Locate every Plasmodium falciparum-infected red blood cell.
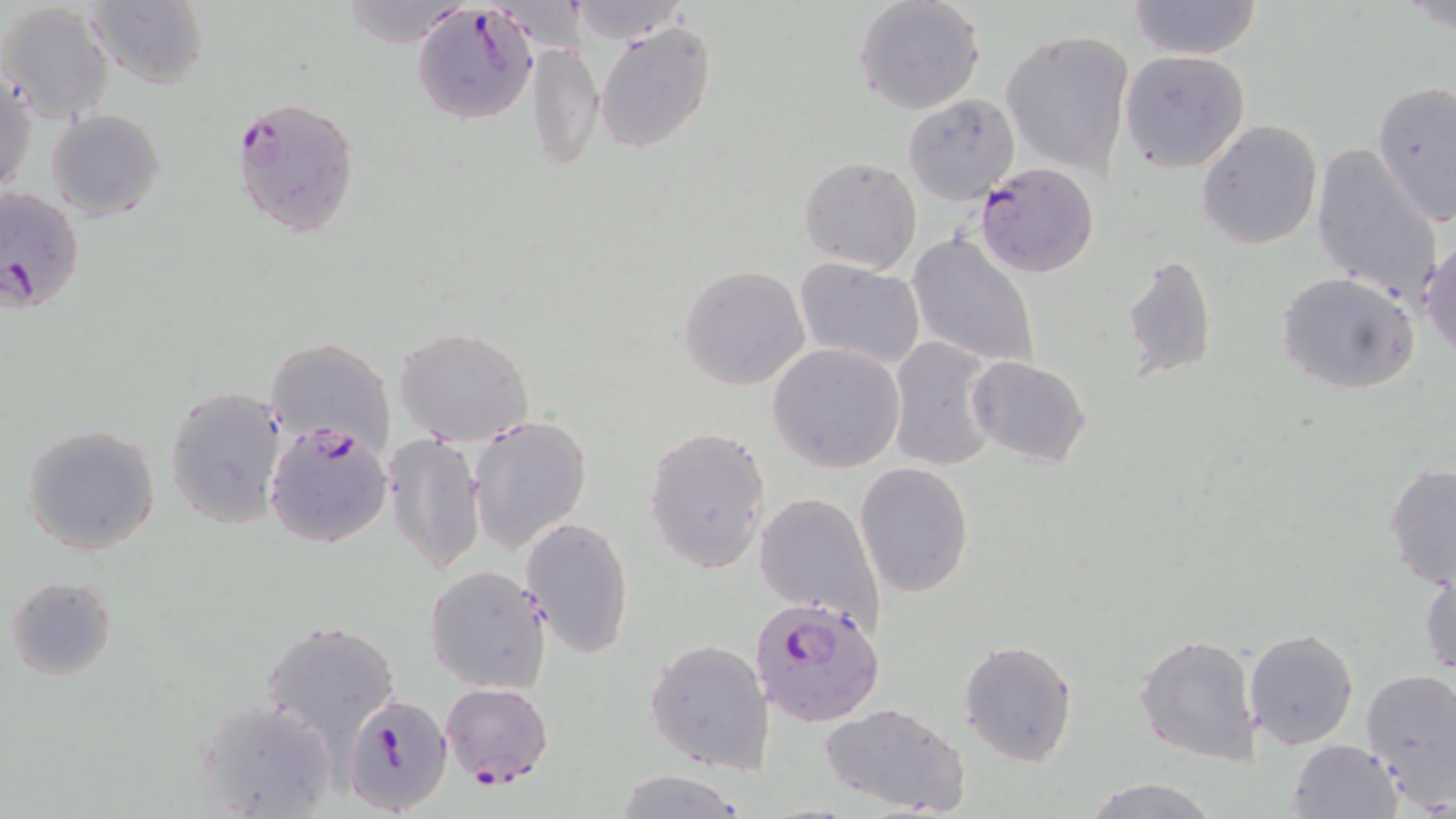

Approximate bounding boxes as [x1, y1, x2, y2] in pixels.
Plasmodium falciparum-infected red blood cells: [412, 3, 545, 127], [229, 94, 360, 237], [975, 161, 1101, 279], [0, 186, 86, 316], [266, 421, 392, 550], [751, 597, 885, 726], [344, 698, 459, 819].

Summary:
  - Uninfected red blood cell locations: [336, 0, 474, 49], [564, 0, 694, 45], [852, 0, 986, 115], [86, 1, 211, 88], [1126, 1, 1264, 62], [1, 2, 113, 122], [593, 20, 717, 155], [998, 30, 1136, 175], [528, 40, 602, 173], [1120, 49, 1252, 174], [1, 72, 35, 199], [1370, 82, 1455, 224], [902, 91, 1018, 204], [47, 109, 164, 222], [1196, 119, 1324, 250], [1311, 143, 1441, 303], [797, 156, 922, 274], [907, 233, 1040, 372], [1420, 236, 1455, 359], [1120, 251, 1218, 382], [795, 261, 925, 370], [678, 264, 810, 391], [1275, 271, 1420, 395], [394, 326, 533, 445], [886, 335, 1004, 473], [267, 338, 397, 452], [769, 344, 905, 473], [966, 355, 1091, 468], [165, 386, 288, 529], [468, 415, 592, 553], [20, 423, 162, 556], [644, 426, 771, 573], [383, 431, 487, 576], [856, 462, 973, 596], [1384, 463, 1456, 592], [754, 490, 885, 629], [520, 515, 635, 658], [1420, 565, 1455, 676], [425, 566, 550, 693], [6, 575, 118, 680], [263, 621, 399, 743], [1243, 628, 1359, 749], [1134, 632, 1260, 765], [645, 637, 774, 774], [958, 638, 1078, 767], [1359, 668, 1456, 807], [440, 682, 554, 787], [196, 696, 339, 815], [822, 701, 972, 817], [1286, 738, 1403, 819], [612, 770, 746, 818], [1079, 776, 1221, 818]
  - Slide-level diagnosis: Plasmodium falciparum
  - Modality: optical microscopy
  - Image size: 1456×819 pixels
  - Magnification: 1000x
  - Stain: May-Grünwald-Giemsa
  - Preparation: thin blood smear
  - Field of view: one of a larger specimen